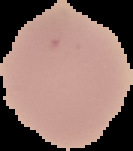

image_size: 133×151 pixels
result: no malaria parasites seen
preparation: thin blood film
image_type: cell region segmented out of the field of view; surrounding area masked to black